State the blood parasite species.
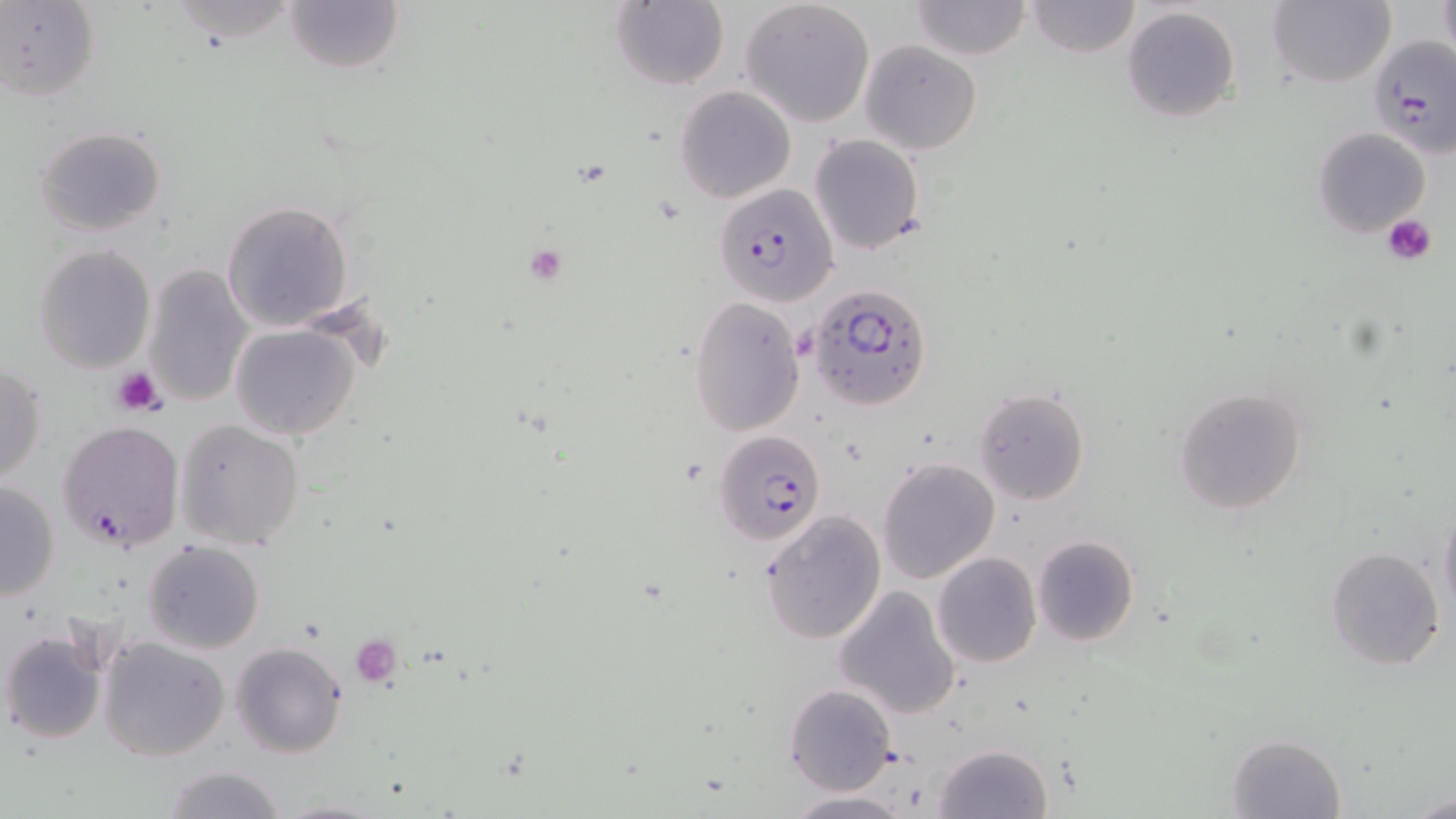

Plasmodium falciparum.

Summary:
  - Coordinate format: approximate bounding boxes as (x1, y1, x2, y2) in pixels
  - Plasmodium falciparum-infected red blood cell locations: (1368, 34, 1455, 154), (713, 184, 840, 308), (808, 281, 932, 413), (57, 420, 185, 552), (714, 427, 829, 541)
  - Platelet locations: (1380, 214, 1439, 266), (110, 365, 164, 416), (351, 636, 400, 685)
  - Uninfected red blood cell locations: (0, 0, 100, 101), (285, 0, 405, 73), (740, 0, 876, 127), (1267, 0, 1394, 88), (608, 1, 730, 90), (909, 1, 1032, 61), (1025, 1, 1141, 58), (1437, 1, 1456, 58), (1123, 6, 1242, 124), (859, 41, 982, 153), (675, 85, 796, 203), (34, 125, 166, 236), (1311, 126, 1431, 238), (809, 134, 925, 255), (221, 200, 353, 331), (34, 244, 156, 373), (144, 263, 251, 408), (689, 295, 806, 437), (231, 325, 362, 442), (0, 363, 46, 486), (1174, 385, 1309, 515), (974, 387, 1090, 504), (177, 419, 305, 550), (878, 457, 1000, 584), (0, 481, 61, 601), (1439, 498, 1456, 628), (760, 511, 886, 645), (1032, 534, 1140, 647), (143, 540, 264, 653), (1327, 546, 1446, 671), (933, 552, 1041, 668), (833, 585, 964, 719), (1, 628, 108, 744), (98, 636, 230, 761), (230, 641, 348, 758), (784, 683, 897, 796), (1225, 733, 1347, 819), (935, 742, 1051, 818), (159, 763, 289, 819), (785, 790, 912, 817), (1411, 790, 1456, 819), (275, 797, 387, 819)
  - Modality: optical microscopy
  - Image size: 1456×819 pixels
  - Magnification: 1000x
  - Stain: May-Grünwald-Giemsa
  - Preparation: thin blood film
  - Field of view: single